Comment on the morphology of the red blood cells.
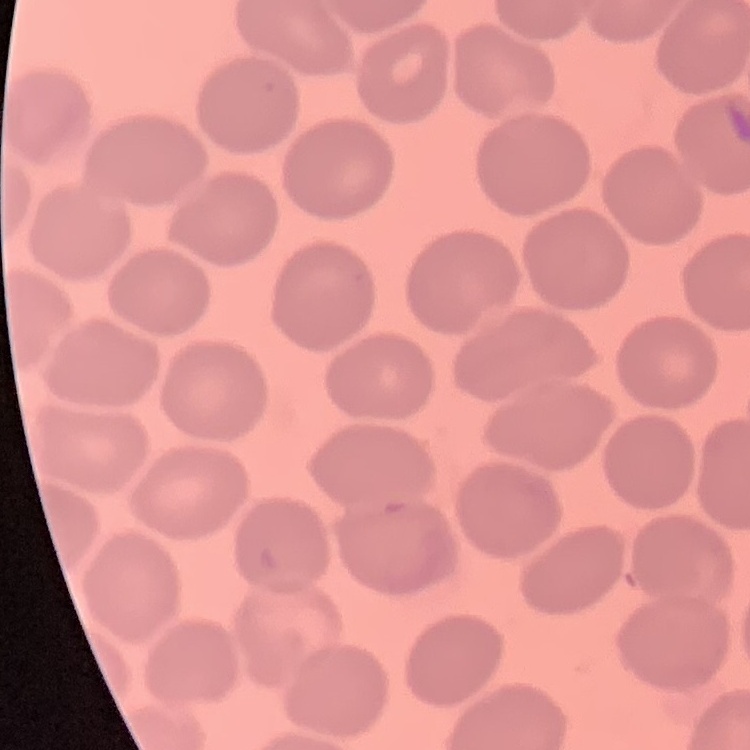

No rouleaux formation.

Summary:
  - Image type: square crop of a larger photomicrograph
  - Preparation: thin blood film
  - Stain: Field's or Giemsa